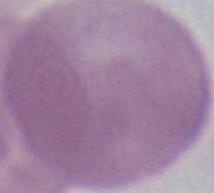
{
  "modality": "photomicrograph",
  "identification": "red blood cell",
  "magnification": "1000x"
}